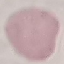
malaria status = uninfected
stain = Giemsa
image type = cell patch, automatically extracted from a larger field of view and resized to 64 × 64 pixels
preparation = thin blood smear
capture = smartphone through the microscope eyepiece